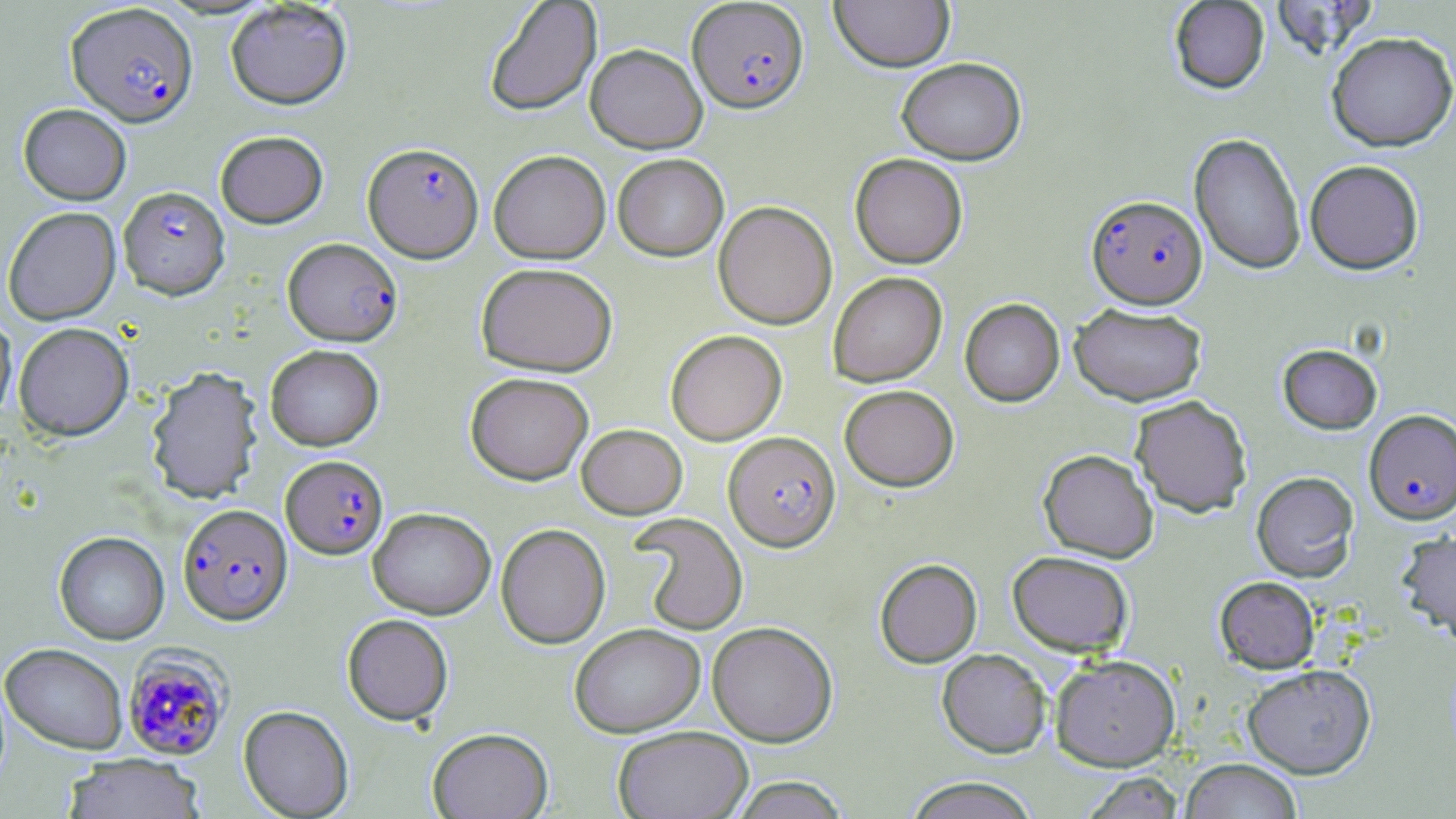
Summary:
  - Coordinate format: approximate bounding boxes as (x1, y1, x2, y2) in pixels
  - Plasmodium falciparum-infected red blood cell locations: (687, 0, 809, 113), (66, 2, 198, 127), (363, 142, 484, 262), (118, 186, 230, 299), (1087, 194, 1207, 308), (283, 237, 402, 346), (1363, 409, 1456, 523), (724, 431, 841, 551), (281, 454, 388, 558), (178, 503, 292, 624), (123, 648, 232, 760)
  - Uninfected red blood cell locations: (830, 0, 955, 72), (1169, 0, 1270, 94), (1268, 0, 1377, 59), (483, 1, 602, 116), (225, 2, 352, 110), (1327, 31, 1456, 151), (585, 43, 707, 153), (896, 57, 1026, 165), (18, 103, 131, 205), (215, 130, 328, 228), (1189, 133, 1306, 275), (488, 149, 611, 263), (612, 153, 728, 260), (849, 153, 968, 268), (1304, 159, 1424, 274), (713, 200, 837, 329), (2, 206, 121, 325), (476, 262, 618, 376), (828, 272, 947, 387), (960, 298, 1065, 406), (1069, 302, 1207, 406), (0, 312, 17, 426), (13, 322, 134, 440), (665, 329, 786, 445), (265, 344, 383, 450), (1277, 344, 1382, 434), (146, 366, 262, 504), (465, 372, 593, 485), (840, 385, 959, 491), (1130, 395, 1253, 517), (577, 424, 687, 518), (1038, 448, 1159, 562), (1251, 470, 1359, 582), (368, 506, 496, 620), (630, 513, 749, 633), (496, 523, 610, 649), (1397, 529, 1456, 642), (54, 531, 169, 644), (1007, 550, 1134, 656), (875, 558, 982, 667), (1214, 576, 1320, 673), (342, 614, 454, 725), (707, 621, 838, 746), (569, 623, 705, 737), (1, 642, 128, 754), (937, 648, 1051, 758), (1050, 654, 1180, 771), (1242, 664, 1376, 778), (239, 705, 354, 818), (613, 725, 753, 819), (427, 727, 553, 819), (60, 754, 207, 819), (1180, 758, 1303, 819), (1080, 772, 1184, 818), (728, 776, 851, 818), (904, 776, 1039, 819)
  - Slide-level diagnosis: Plasmodium falciparum
  - Preparation: thin blood smear
  - Stain: May-Grünwald-Giemsa
  - Modality: optical microscopy
  - Field of view: one of a larger specimen
  - Image size: 1456×819 pixels
  - Magnification: 1000x